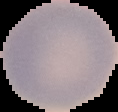

Summary:
  - Result: no Plasmodium parasites detected
  - Preparation: thin blood film
  - Image type: segmented cell region on a black background
  - Image size: 118×112 pixels